Assess this cell for malaria.
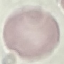

Uninfected.

Automatically extracted cell patch, resized to 64 × 64 pixels. Thin blood film. Acquired by smartphone through the microscope eyepiece. Giemsa stain.